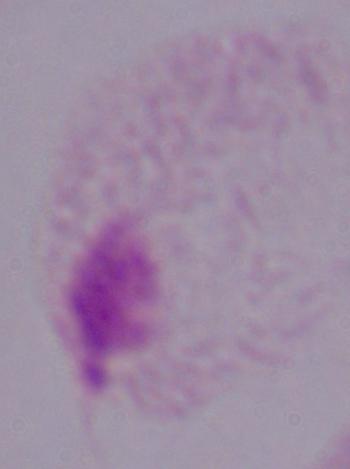
Summary:
  - Modality: micrograph
  - Identification: trichomonad
  - Magnification: 1000x